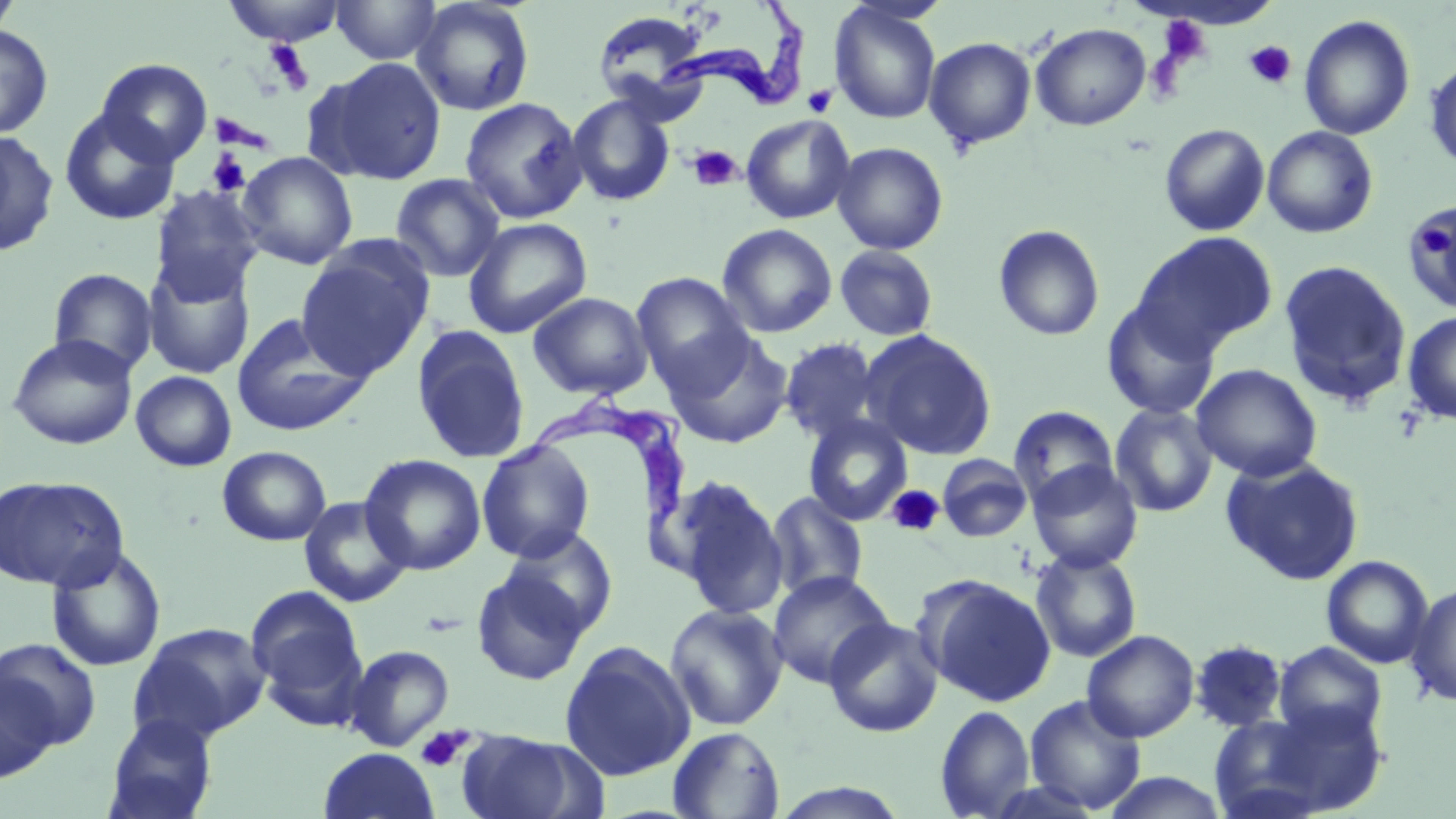

Approximate bounding boxes as (x1,y1)-(x2,y2) corner pairs in pixels. Trypanosoma brucei locations: (657,1)-(809,113), (511,388)-(691,543). Platelet locations: (1157,15)-(1211,66), (1244,40)-(1297,89), (263,41)-(315,91), (803,85)-(836,117), (216,114)-(264,149), (689,145)-(743,191), (207,150)-(252,196), (1422,222)-(1450,257), (886,485)-(945,537), (415,725)-(472,772). Uninfected red blood cell locations: (0,0)-(22,41), (224,0)-(346,46), (331,0)-(442,65), (411,0)-(535,117), (829,2)-(942,125), (591,10)-(711,112), (1299,15)-(1415,141), (1030,23)-(1151,131), (0,25)-(54,139), (924,36)-(1036,151), (315,57)-(448,184), (96,58)-(213,166), (1424,59)-(1456,172), (567,94)-(675,206), (459,96)-(587,223), (59,108)-(180,225), (740,114)-(856,224), (1159,123)-(1270,236), (1261,126)-(1379,238), (0,129)-(59,257), (831,141)-(948,255), (237,151)-(358,269), (389,173)-(506,282), (149,186)-(263,304), (1404,203)-(1456,313), (463,217)-(592,338), (717,223)-(838,338), (993,224)-(1105,341), (1134,231)-(1278,353), (296,241)-(433,379), (835,244)-(939,341), (142,258)-(255,379), (1278,260)-(1412,408), (48,268)-(158,377), (631,272)-(752,388), (528,291)-(653,400), (1102,297)-(1220,419), (1402,310)-(1456,425), (232,313)-(374,436), (411,325)-(531,464), (664,330)-(793,449), (862,330)-(997,460), (7,334)-(138,450), (779,337)-(883,446), (1191,363)-(1322,482), (131,371)-(237,471), (1110,403)-(1219,517), (1008,405)-(1119,508), (803,415)-(912,526), (476,439)-(595,563), (217,446)-(331,546), (360,453)-(486,575), (937,454)-(1033,542), (1222,457)-(1364,585), (1028,461)-(1143,574), (667,474)-(789,620), (0,475)-(129,591), (765,491)-(869,602), (298,496)-(412,608), (501,527)-(618,638), (45,546)-(167,673), (1030,549)-(1142,662), (1321,555)-(1434,669), (470,567)-(591,685), (767,569)-(894,688), (917,575)-(1057,707), (1405,582)-(1456,706), (245,584)-(368,720), (664,603)-(788,731), (824,617)-(944,738), (129,622)-(272,745), (1082,629)-(1199,742), (0,638)-(102,750), (559,640)-(695,781), (1189,640)-(1289,732), (1273,642)-(1387,742), (344,644)-(455,751), (0,670)-(60,783), (1024,694)-(1147,814), (1250,700)-(1391,815), (935,705)-(1036,818), (1210,711)-(1333,819), (102,713)-(219,819), (668,726)-(785,818), (457,730)-(591,819), (317,747)-(441,818), (1101,772)-(1230,818), (769,783)-(911,819). Slide-level diagnosis: Trypanosoma brucei. Image is 1456×819 pixels. Captured at 1000x magnification. Thin blood film. May-Grünwald-Giemsa-stained preparation. Light microscopy. Single field of view.